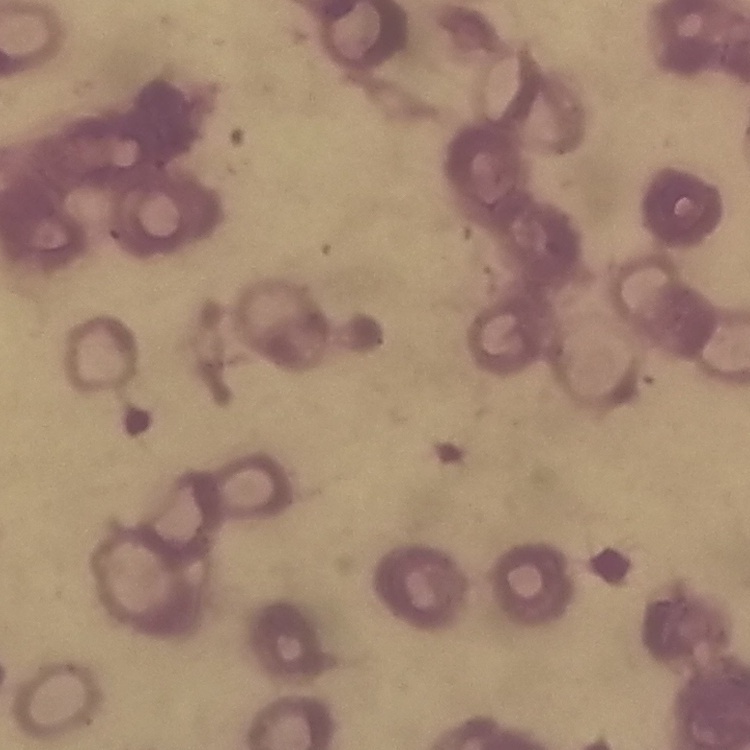

Summary:
  - Erythrocyte morphology: rouleaux formation
  - Image type: one tile cut from a larger photomicrograph
  - Preparation: thin blood film
  - Stain: Field's or Giemsa